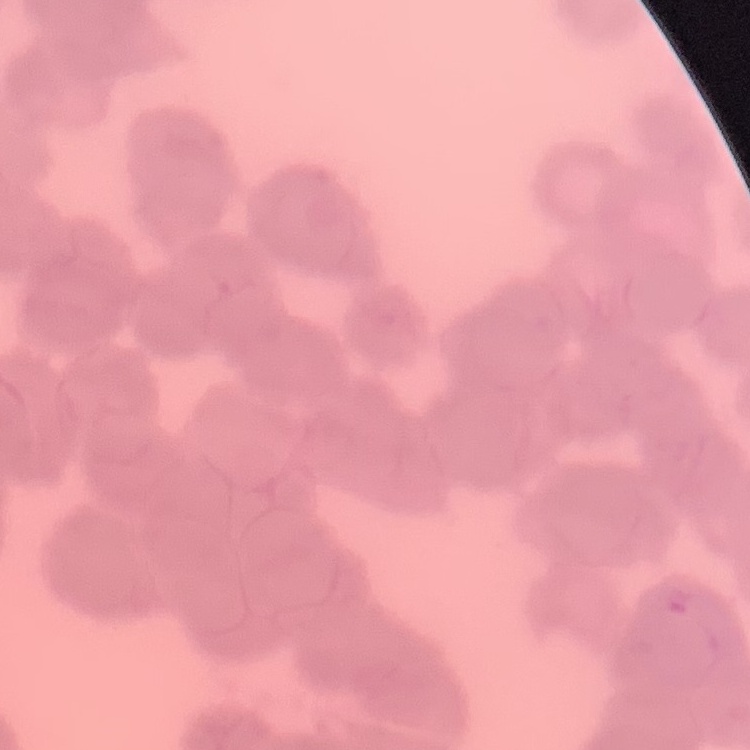
The erythrocytes exhibit rouleaux formation. One tile cut from a larger photomicrograph. Field's or Giemsa stain. Thin peripheral smear.